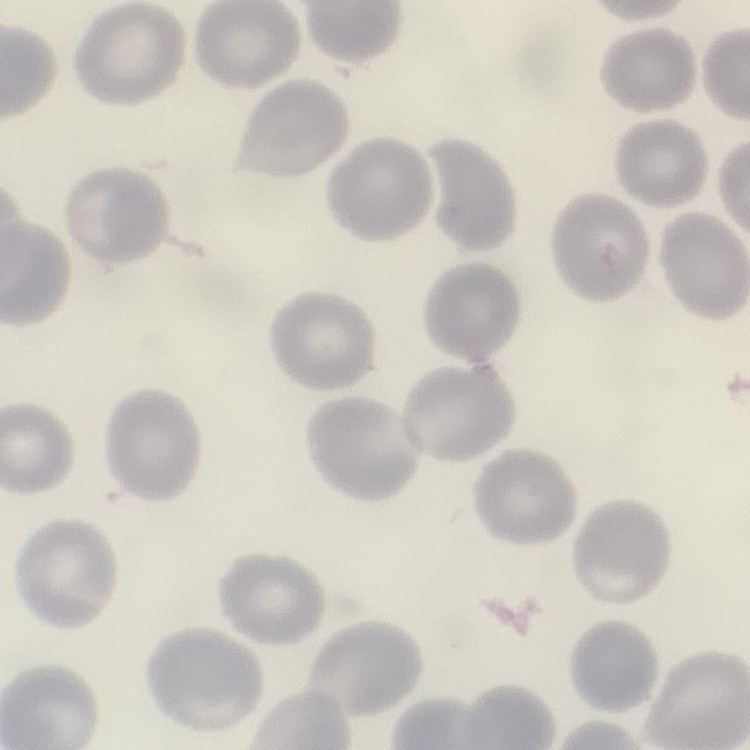

The erythrocytes show no rouleaux formation. One tile cut from a larger photomicrograph. Field's or Giemsa stain. Thin blood film.